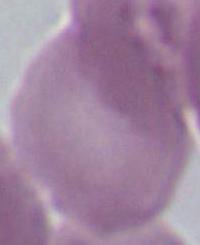

Summary:
  - Magnification: 1000x
  - Modality: micrograph
  - Identification: erythrocyte